Name the parasite shown.
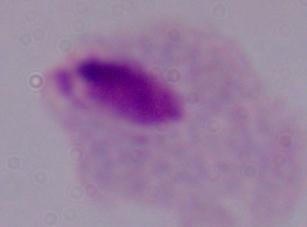

A trichomonad.

Captured at 1000x magnification. Photomicrograph.